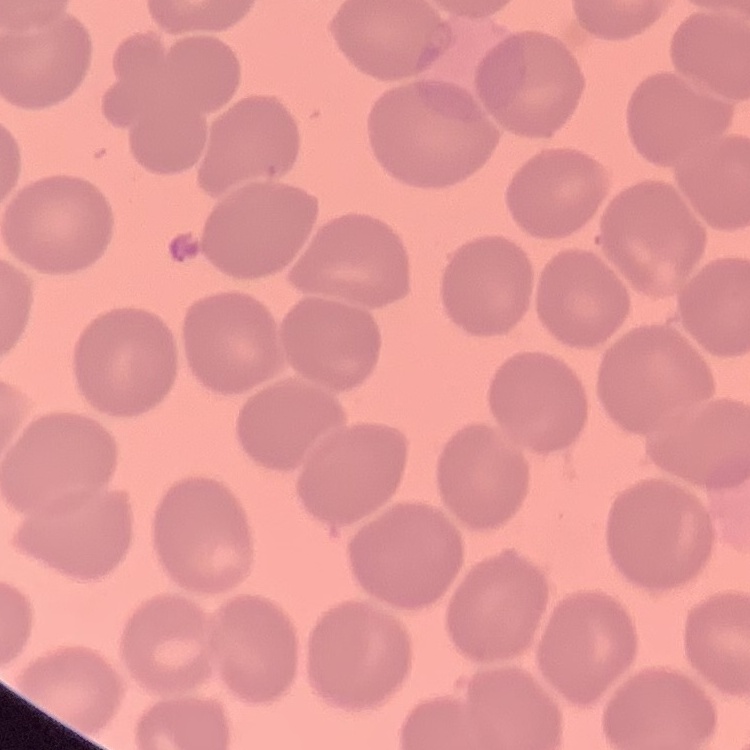
Summary:
  - Erythrocyte morphology: no rouleaux formation
  - Stain: Field's or Giemsa
  - Image type: one tile cut from a larger photomicrograph
  - Preparation: thin blood film